Comment on the morphology of the red blood cells.
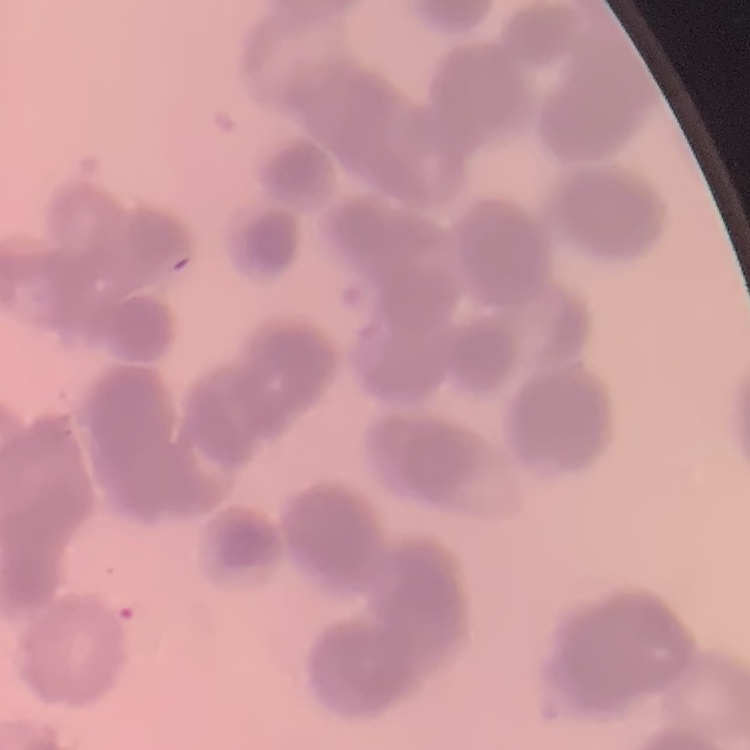

Rouleaux formation.

One tile cut from a larger photomicrograph. Field's or Giemsa stain. Thin blood film.